Classify this cell by malaria status.
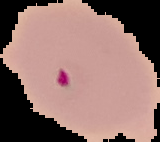

It is parasitized.

Summary:
  - Image type: segmented cell region with the area outside set to black
  - Image size: 160×142 pixels
  - Preparation: thin blood film